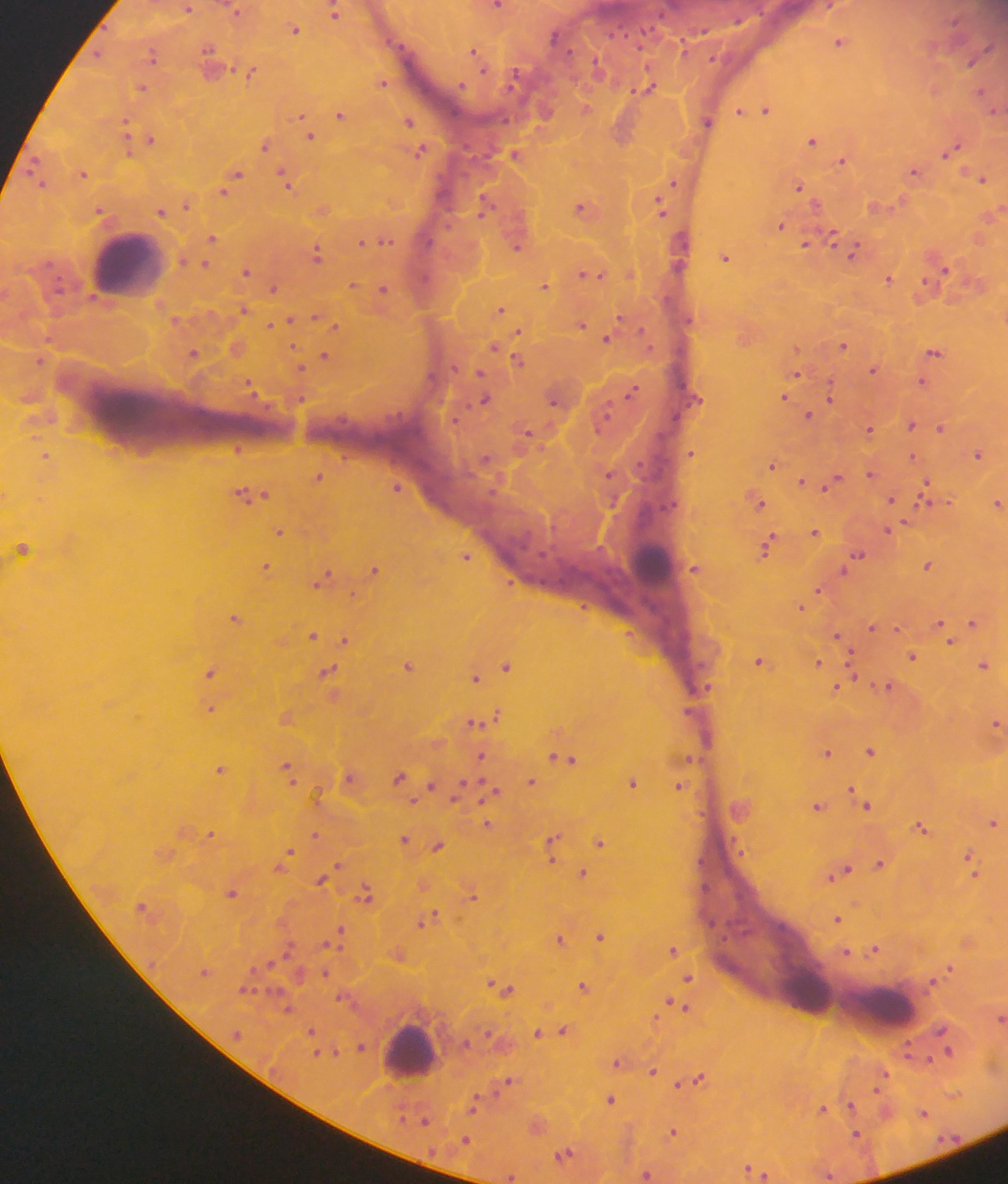 Approximate centers as {x, y} in pixels. Malaria parasite locations: {496, 6}, {827, 6}, {188, 8}, {236, 10}, {333, 12}, {294, 29}, {840, 41}, {475, 52}, {97, 54}, {152, 55}, {209, 60}, {251, 71}, {382, 82}, {141, 88}, {648, 88}, {981, 92}, {585, 109}, {765, 109}, {739, 110}, {339, 114}, {301, 116}, {408, 121}, {707, 121}, {126, 128}, {310, 135}, {150, 139}, {812, 140}, {265, 145}, {950, 149}, {418, 151}, {515, 154}, {842, 160}, {914, 171}, {83, 173}, {235, 174}, {980, 178}, {286, 180}, {673, 183}, {799, 186}, {224, 190}, {186, 204}, {660, 206}, {581, 207}, {483, 208}, {322, 209}, {100, 211}, {160, 211}, {780, 225}, {833, 236}, {212, 237}, {385, 239}, {363, 243}, {806, 243}, {516, 246}, {853, 252}, {316, 254}, {725, 257}, {204, 264}, {941, 268}, {246, 271}, {629, 274}, {588, 275}, {888, 278}, {353, 285}, {545, 286}, {273, 288}, {383, 289}, {499, 309}, {242, 311}, {176, 321}, {286, 322}, {274, 324}, {581, 324}, {333, 326}, {519, 332}, {607, 338}, {843, 345}, {236, 348}, {496, 348}, {934, 351}, {192, 353}, {324, 356}, {517, 359}, {40, 360}, {300, 367}, {872, 370}, {795, 374}, {922, 382}, {249, 386}, {632, 391}, {829, 392}, {783, 397}, {484, 399}, {554, 400}, {808, 415}, {911, 425}, {940, 428}, {869, 429}, {528, 434}, {237, 447}, {691, 453}, {977, 453}, {46, 456}, {772, 465}, {609, 473}, {870, 473}, {318, 477}, {801, 482}, {831, 482}, {396, 487}, {925, 492}, {247, 494}, {892, 500}, {756, 501}, {997, 503}, {279, 531}, {889, 531}, {813, 532}, {767, 546}, {22, 549}, {465, 556}, {855, 556}, {927, 565}, {266, 567}, {695, 568}, {374, 569}, {322, 579}, {818, 589}, {801, 607}, {235, 618}, {973, 622}, {871, 628}, {943, 628}, {312, 635}, {344, 639}, {839, 639}, {912, 656}, {760, 662}, {818, 663}, {408, 665}, {983, 665}, {506, 666}, {210, 672}, {327, 672}, {475, 677}, {885, 686}, {836, 687}, {210, 709}, {286, 717}, {493, 717}, {480, 720}, {996, 723}, {870, 750}, {827, 752}, {481, 756}, {688, 758}, {566, 759}, {220, 769}, {288, 770}, {350, 777}, {399, 777}, {531, 782}, {632, 782}, {430, 786}, {678, 786}, {490, 792}, {865, 803}, {817, 806}, {993, 822}, {487, 824}, {921, 827}, {209, 834}, {314, 835}, {404, 838}, {600, 842}, {552, 843}, {438, 845}, {286, 855}, {970, 862}, {880, 864}, {338, 867}, {972, 872}, {583, 873}, {840, 873}, {322, 878}, {231, 893}, {365, 895}, {472, 895}, {434, 916}, {837, 918}, {426, 921}, {339, 934}, {600, 935}, {560, 939}, {673, 949}, {874, 949}, {846, 952}, {949, 968}, {324, 973}, {688, 978}, {503, 987}, {584, 987}, {676, 1005}, {287, 1008}, {1000, 1018}, {563, 1030}, {310, 1031}, {537, 1032}, {360, 1046}, {946, 1051}, {618, 1062}, {652, 1071}, {699, 1077}, {882, 1077}, {508, 1080}, {678, 1083}, {610, 1099}, {474, 1102}, {851, 1105}, {823, 1109}, {923, 1113}, {425, 1119}, {537, 1125}, {672, 1132}, {857, 1136}, {465, 1140}, {564, 1155}, {751, 1170}, {646, 1173}, {760, 1173}, {828, 1174}, {510, 1177}. Leukocyte locations: {126, 262}, {651, 565}, {807, 992}, {886, 1008}, {410, 1051}. Single field of view. Image is 1008×1184 pixels. Sample from Ghana. Mobile-phone photograph taken through the microscope. Thick blood smear.